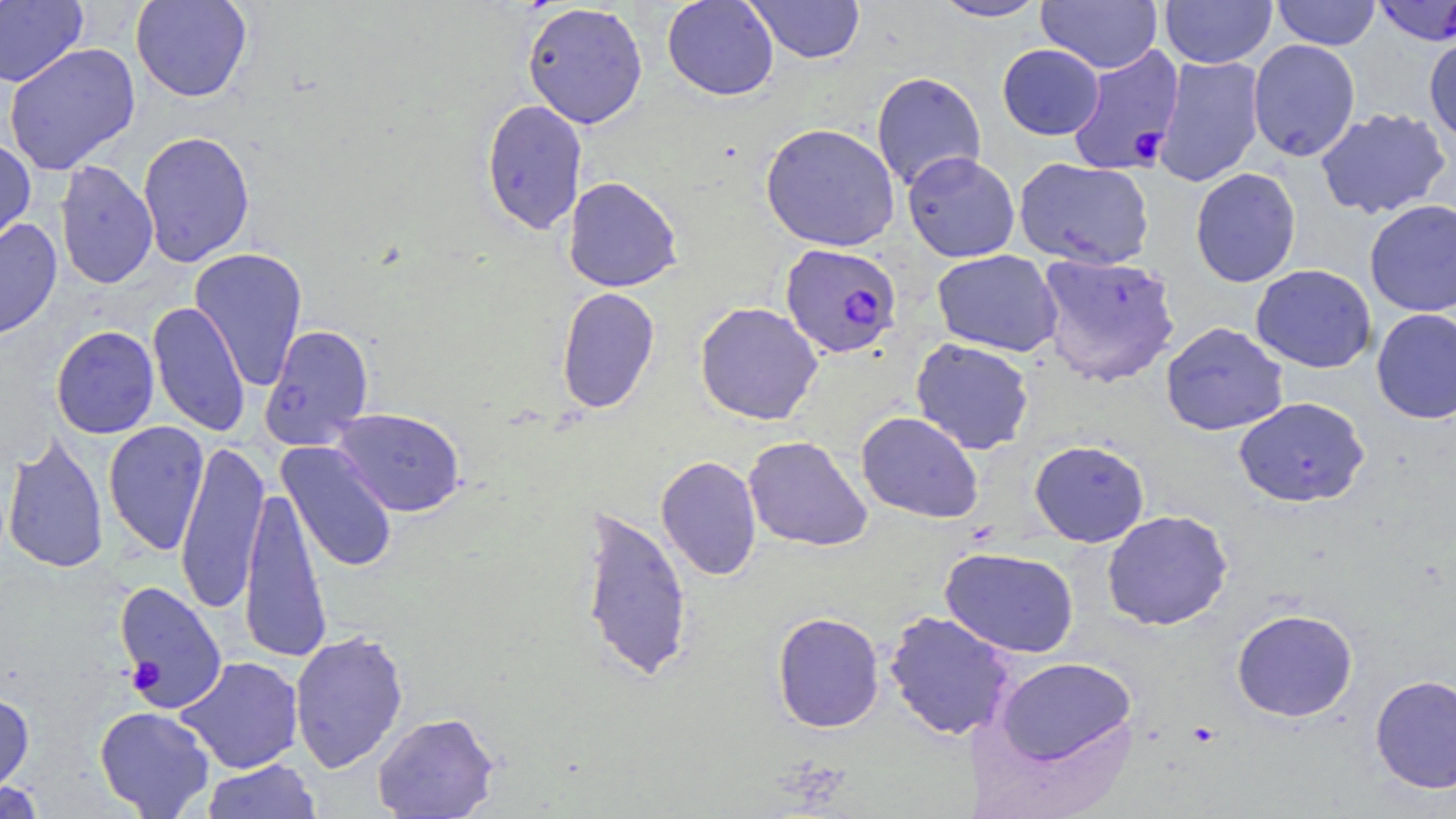 Approximate bounding boxes as [x1, y1, x2, y2] in pixels. Plasmodium falciparum-infected red blood cell locations (subset): [1066, 44, 1185, 175], [780, 242, 903, 358], [114, 580, 227, 713]. Uninfected red blood cell locations (subset): [130, 0, 253, 102], [662, 0, 779, 101], [743, 0, 866, 64], [931, 0, 1048, 22], [1160, 0, 1276, 69], [1271, 0, 1381, 50], [0, 1, 88, 87], [1036, 1, 1162, 73], [521, 2, 648, 129], [1423, 33, 1456, 145], [1247, 39, 1361, 161], [3, 42, 141, 175], [997, 44, 1104, 140], [1153, 55, 1265, 187], [871, 71, 987, 191], [480, 98, 588, 235], [1315, 108, 1452, 219], [760, 122, 901, 252], [137, 130, 255, 267], [0, 136, 36, 250], [902, 151, 1020, 262], [1014, 157, 1155, 270], [54, 160, 159, 289], [1189, 167, 1302, 288], [563, 176, 683, 292], [1364, 199, 1456, 317], [0, 218, 62, 341], [189, 247, 308, 391], [931, 249, 1062, 357], [1036, 253, 1181, 388], [1250, 264, 1377, 373], [555, 287, 661, 414], [147, 301, 251, 437], [694, 301, 823, 425], [1371, 308, 1456, 424], [1160, 322, 1288, 435], [260, 323, 375, 450], [51, 325, 159, 439], [911, 338, 1035, 454], [1234, 396, 1370, 507], [331, 408, 467, 517], [856, 411, 984, 523], [103, 420, 209, 556], [3, 431, 108, 575], [743, 435, 873, 552], [175, 439, 269, 614], [1029, 440, 1149, 547], [277, 441, 398, 573], [656, 455, 762, 581], [238, 484, 332, 664], [577, 503, 694, 683], [1101, 509, 1233, 631], [940, 547, 1080, 658], [1231, 608, 1358, 722], [884, 610, 1016, 740], [771, 611, 885, 733], [289, 628, 409, 773], [993, 655, 1138, 767], [176, 656, 304, 774], [1370, 673, 1456, 794], [0, 690, 34, 800], [94, 706, 215, 818], [372, 711, 500, 819], [200, 759, 323, 818], [1, 780, 50, 817]. Slide-level diagnosis: Plasmodium falciparum. Light microscopy. Image is 1456×819 pixels. May-Grünwald-Giemsa stain. 1000x magnification. Thin blood film. Single field of view.